Assess this cell for malaria.
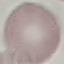

It is uninfected.

Summary:
  - Capture: smartphone camera at the microscope eyepiece
  - Stain: Giemsa
  - Image type: automatically extracted cell patch, resized to 64 × 64 pixels
  - Preparation: thin blood smear